Give the position of every leukocyte visible.
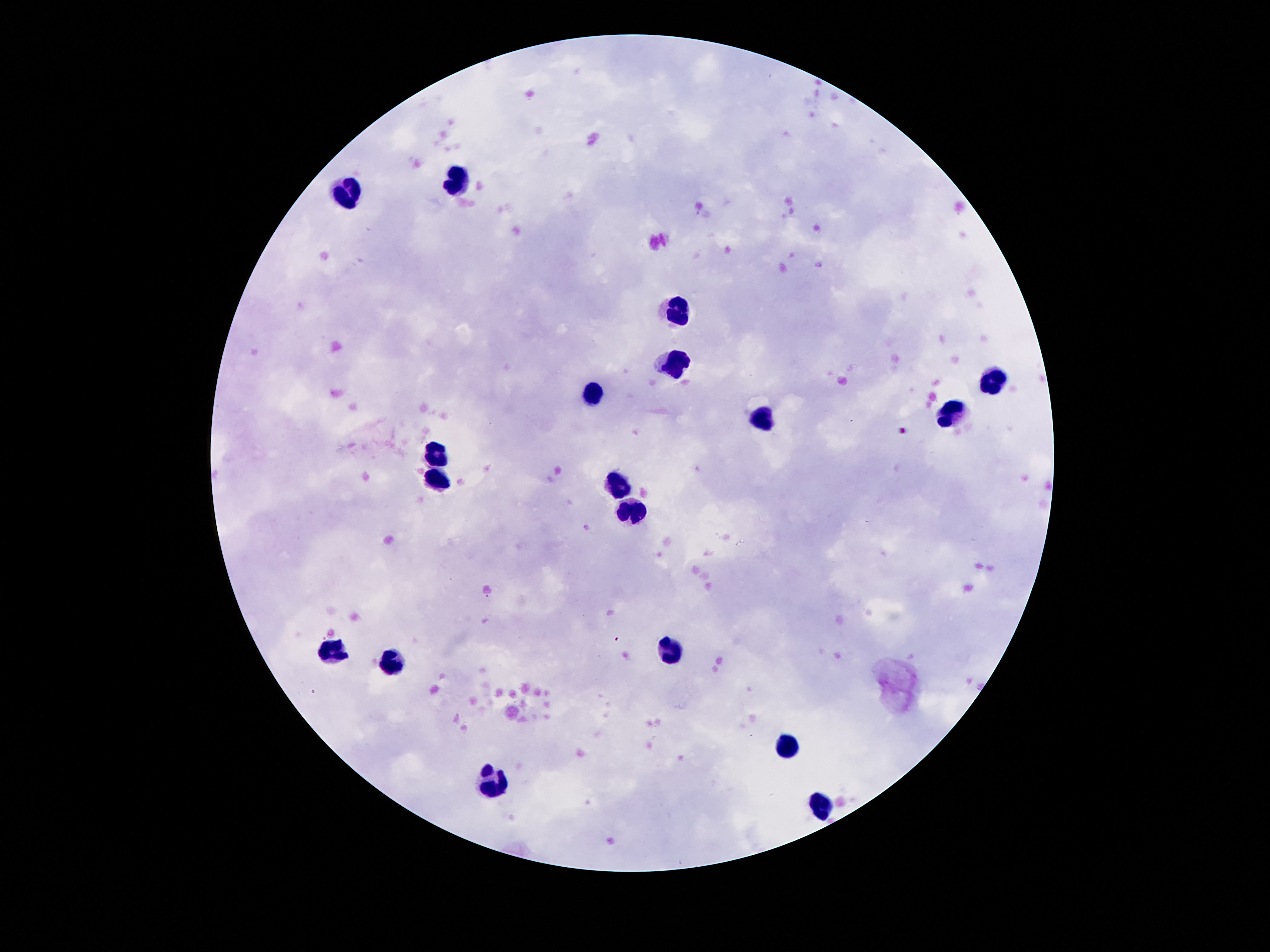

Approximate object centers, in pixels from the top-left corner.
Leukocytes: (x=455, y=182), (x=345, y=192), (x=673, y=312), (x=673, y=359), (x=993, y=382), (x=595, y=398), (x=953, y=412), (x=761, y=418), (x=441, y=452), (x=433, y=479), (x=615, y=486), (x=627, y=510), (x=331, y=644), (x=670, y=651), (x=391, y=664), (x=786, y=746), (x=492, y=786), (x=823, y=806).

Image is 1270×952 pixels. Thick peripheral-blood smear. Giemsa-stained preparation. Photographed through the microscope eyepiece with a smartphone camera. One field from this slide. Patient malaria status: negative. 100x magnification.